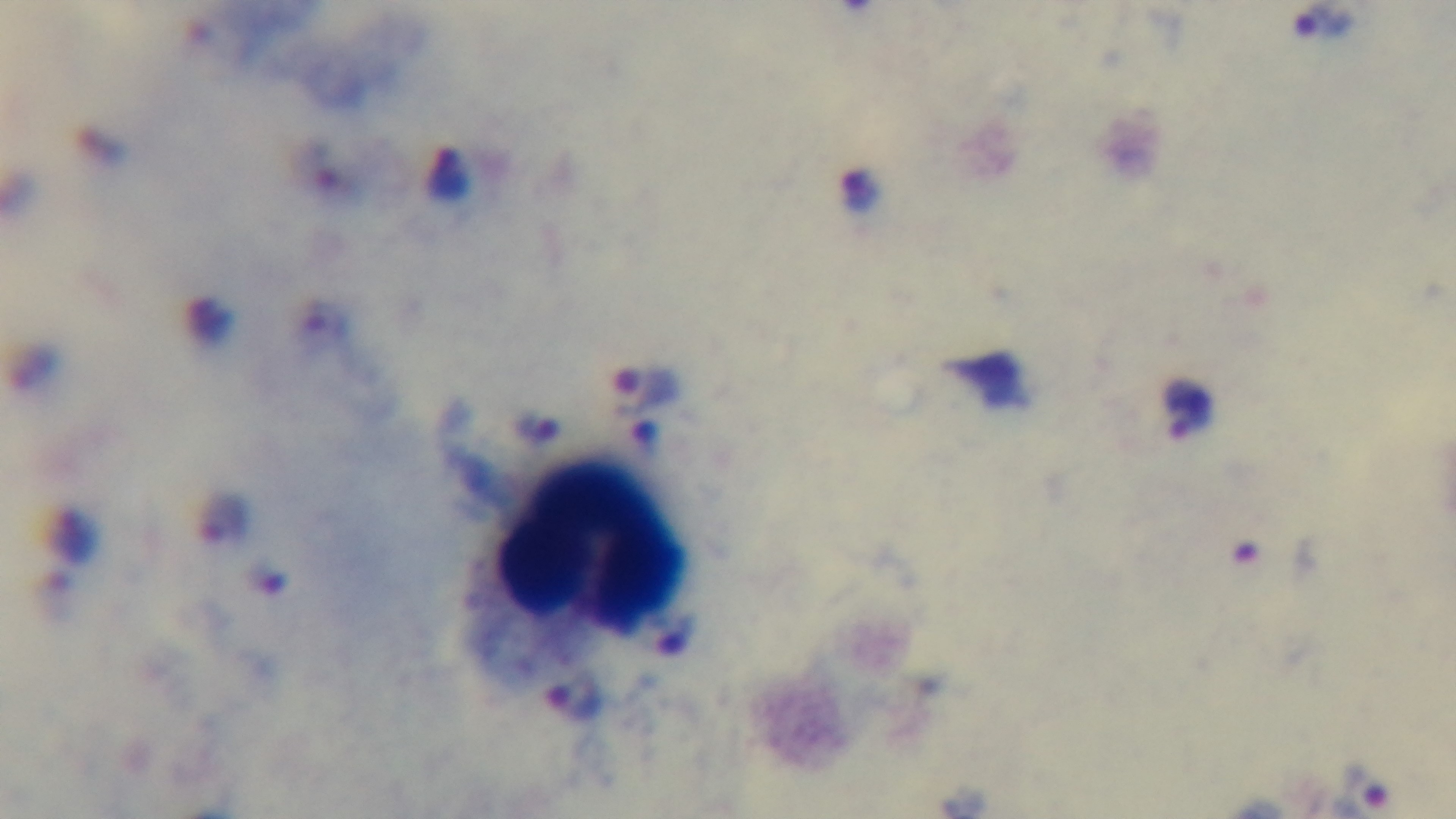
Summary:
  - Field of view: one from the slide
  - Preparation: thick blood film
  - Stain: Giemsa
  - Modality: light microscopy
  - Capture: mounted 4K digital camera
  - Malaria status: positive
  - Objective: 100x oil immersion